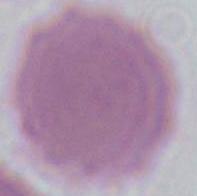

identification: erythrocyte
magnification: 1000x
modality: photomicrograph